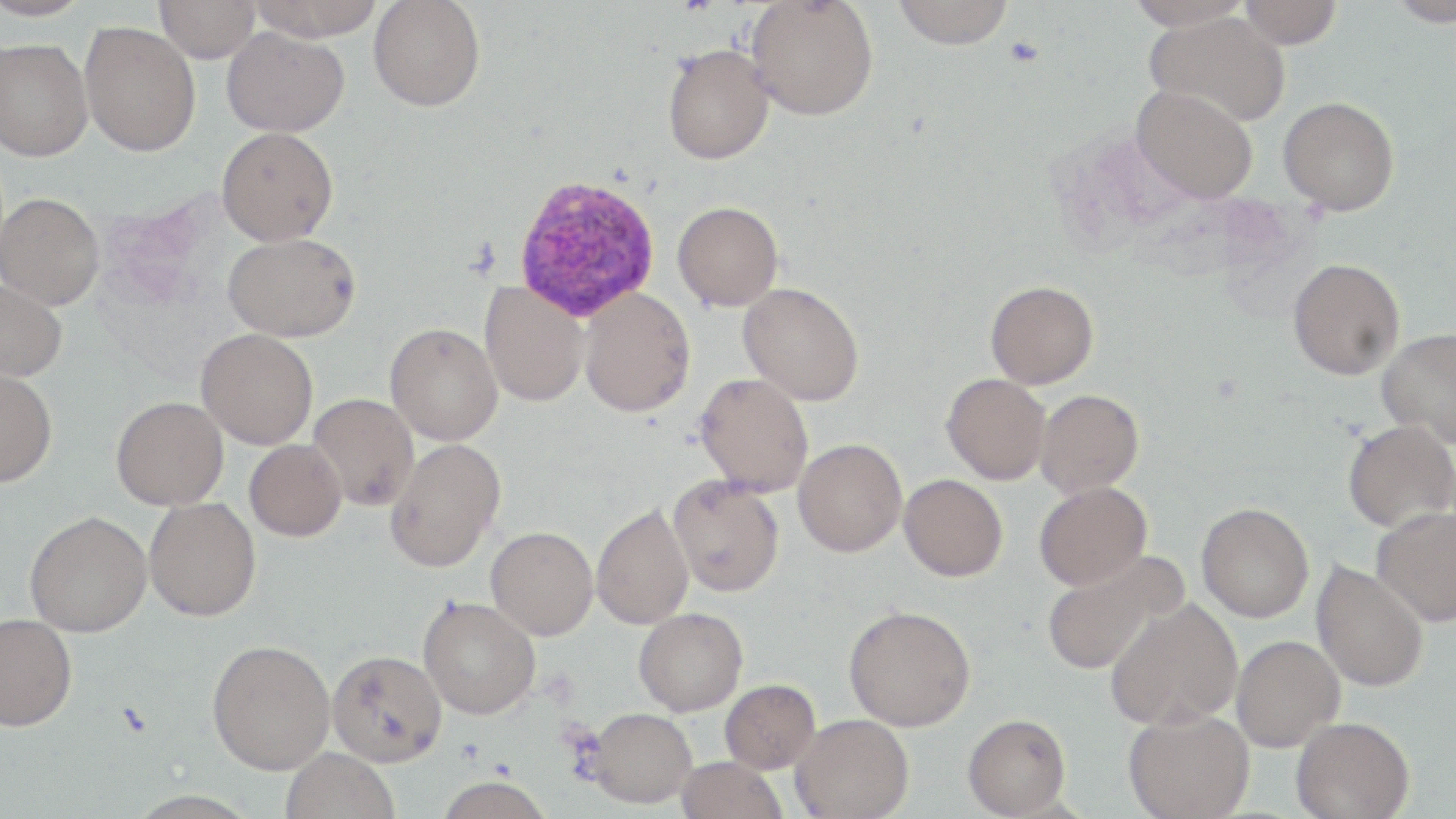
Summary:
  - Coordinate format: approximate bounding boxes as named x1/y1/x2/y2 corners in pixels
  - Plasmodium vivax-infected red blood cell locations: (x1=513, y1=173, x2=661, y2=321)
  - Uninfected red blood cell locations: (x1=0, y1=0, x2=96, y2=20), (x1=155, y1=0, x2=261, y2=62), (x1=246, y1=0, x2=386, y2=41), (x1=746, y1=0, x2=879, y2=120), (x1=1125, y1=0, x2=1255, y2=31), (x1=1237, y1=0, x2=1342, y2=49), (x1=1385, y1=0, x2=1456, y2=27), (x1=368, y1=1, x2=486, y2=112), (x1=892, y1=1, x2=1014, y2=49), (x1=1145, y1=11, x2=1290, y2=126), (x1=79, y1=20, x2=201, y2=157), (x1=221, y1=26, x2=350, y2=137), (x1=0, y1=37, x2=93, y2=161), (x1=662, y1=43, x2=774, y2=164), (x1=1132, y1=86, x2=1258, y2=203), (x1=1278, y1=96, x2=1399, y2=215), (x1=216, y1=127, x2=339, y2=245), (x1=0, y1=192, x2=104, y2=309), (x1=672, y1=201, x2=783, y2=311), (x1=223, y1=232, x2=360, y2=341), (x1=1287, y1=257, x2=1404, y2=380), (x1=0, y1=278, x2=68, y2=381), (x1=985, y1=280, x2=1099, y2=388), (x1=479, y1=281, x2=590, y2=407), (x1=738, y1=282, x2=864, y2=406), (x1=578, y1=288, x2=696, y2=417), (x1=385, y1=322, x2=503, y2=445), (x1=1377, y1=327, x2=1456, y2=446), (x1=196, y1=328, x2=318, y2=449), (x1=0, y1=368, x2=57, y2=487), (x1=694, y1=372, x2=814, y2=496), (x1=942, y1=373, x2=1051, y2=485), (x1=1035, y1=389, x2=1143, y2=496), (x1=308, y1=393, x2=420, y2=511), (x1=111, y1=396, x2=229, y2=510), (x1=1342, y1=420, x2=1456, y2=532), (x1=386, y1=438, x2=506, y2=573), (x1=793, y1=438, x2=907, y2=557), (x1=244, y1=439, x2=347, y2=542), (x1=667, y1=474, x2=784, y2=597), (x1=899, y1=474, x2=1008, y2=581), (x1=1034, y1=482, x2=1152, y2=590), (x1=145, y1=497, x2=262, y2=622), (x1=591, y1=502, x2=694, y2=629), (x1=1196, y1=502, x2=1314, y2=622), (x1=1371, y1=505, x2=1456, y2=626), (x1=24, y1=510, x2=151, y2=637), (x1=485, y1=526, x2=598, y2=640), (x1=1041, y1=550, x2=1186, y2=676), (x1=1311, y1=560, x2=1429, y2=693), (x1=417, y1=595, x2=541, y2=719), (x1=1105, y1=597, x2=1242, y2=731), (x1=843, y1=604, x2=975, y2=731), (x1=633, y1=607, x2=748, y2=716), (x1=0, y1=613, x2=77, y2=731), (x1=1230, y1=634, x2=1344, y2=752), (x1=207, y1=638, x2=335, y2=774), (x1=326, y1=649, x2=447, y2=767), (x1=719, y1=678, x2=820, y2=774), (x1=583, y1=707, x2=697, y2=808), (x1=1124, y1=707, x2=1255, y2=819), (x1=963, y1=713, x2=1071, y2=817), (x1=791, y1=714, x2=914, y2=819), (x1=1291, y1=716, x2=1414, y2=818), (x1=280, y1=747, x2=399, y2=819), (x1=676, y1=757, x2=787, y2=819), (x1=435, y1=777, x2=555, y2=819)
  - Slide-level diagnosis: Plasmodium vivax
  - Magnification: 1000x
  - Image size: 1456×819 pixels
  - Preparation: thin blood smear
  - Field of view: single
  - Stain: May-Grünwald-Giemsa
  - Modality: light microscopy